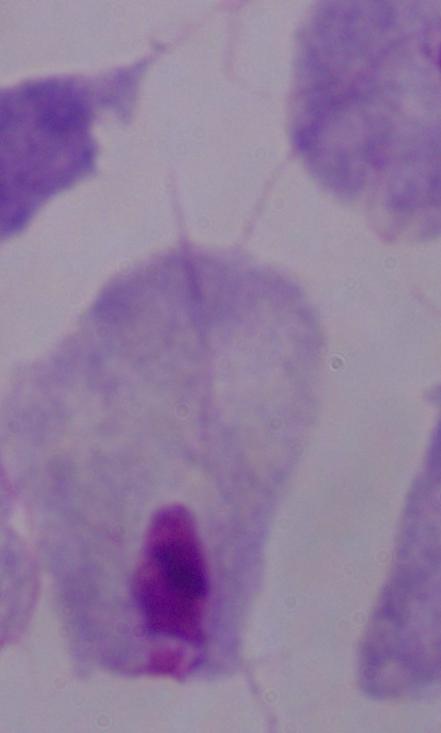
Summary:
  - Magnification: 1000x
  - Modality: photomicrograph
  - Identification: trichomonad